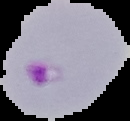
Summary:
  - Image type: segmented cell region with the area outside set to black
  - Preparation: thin blood smear
  - Image size: 130×121 pixels
  - Result: Plasmodium parasites identified